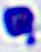
Micrograph. Captured at 400x magnification. A white blood cell is seen.